Give the extent of all uninfected red blood cells.
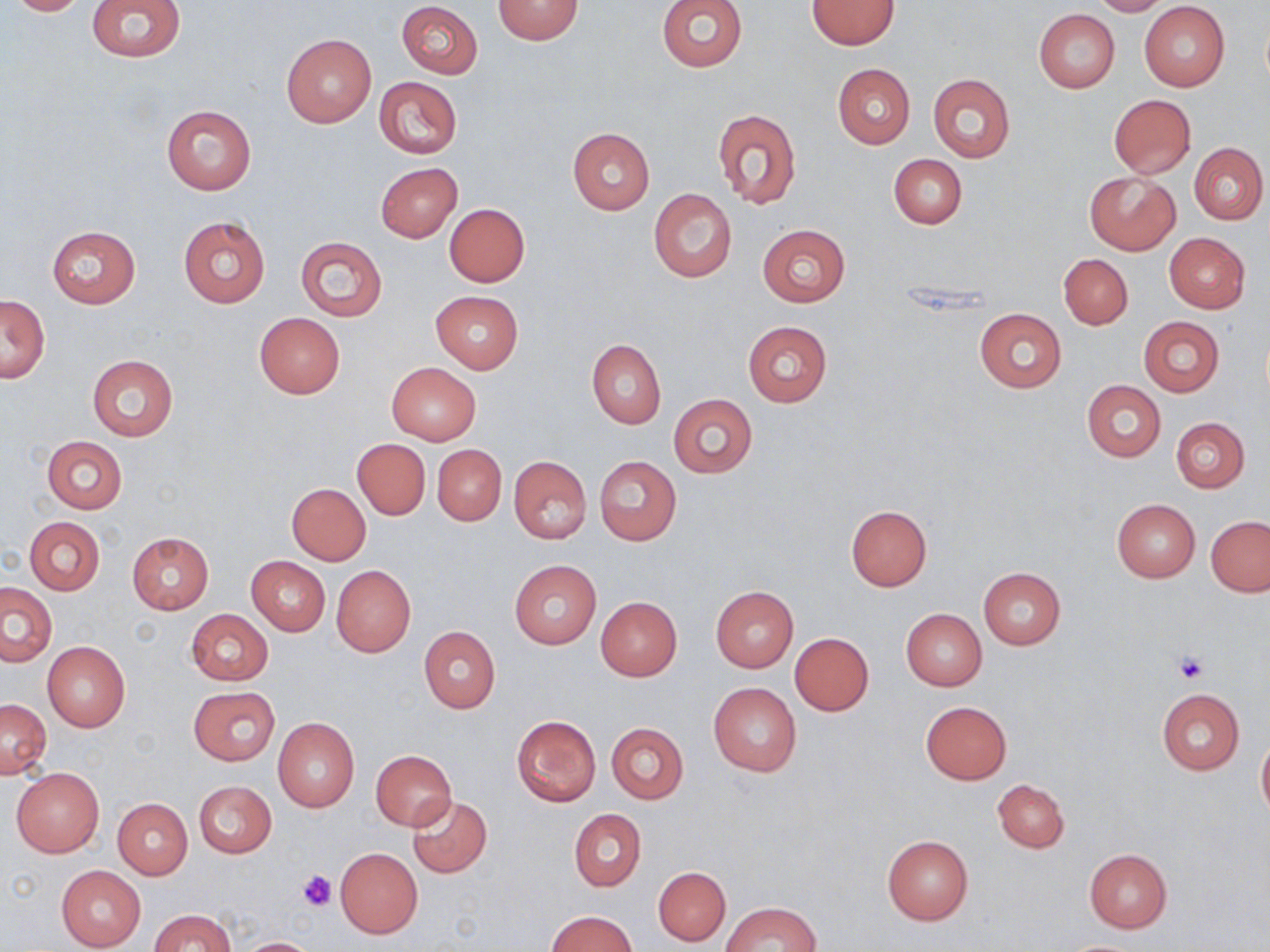

Approximate bounding boxes as [x1, y1, x2, y2] in pixels.
Uninfected red blood cells: [6, 0, 93, 16], [86, 0, 185, 61], [493, 0, 583, 43], [657, 0, 747, 72], [1090, 0, 1172, 16], [806, 1, 899, 50], [397, 2, 484, 78], [1139, 3, 1230, 92], [1034, 9, 1120, 93], [281, 34, 375, 128], [832, 63, 915, 149], [928, 74, 1015, 162], [372, 76, 461, 159], [1108, 94, 1196, 178], [161, 105, 256, 195], [712, 109, 802, 210], [568, 128, 655, 215], [1189, 142, 1268, 224], [888, 154, 966, 229], [375, 162, 462, 242], [1085, 172, 1180, 254], [649, 189, 737, 283], [444, 203, 530, 286], [177, 214, 271, 309], [758, 224, 851, 306], [47, 226, 139, 308], [1164, 233, 1250, 313], [294, 235, 389, 321], [1058, 253, 1133, 329], [431, 291, 523, 372], [1, 295, 50, 384], [973, 308, 1066, 394], [255, 312, 345, 399], [1138, 315, 1224, 397], [743, 321, 833, 407], [587, 340, 665, 428], [87, 354, 177, 441], [386, 362, 481, 444], [1081, 379, 1166, 462], [667, 394, 758, 479], [1171, 417, 1249, 492], [42, 435, 127, 513], [352, 439, 430, 519], [433, 444, 507, 526], [510, 455, 592, 543], [594, 455, 681, 546], [287, 483, 371, 565], [1111, 499, 1200, 581], [845, 505, 932, 592], [1206, 516, 1270, 596], [25, 517, 105, 595], [127, 532, 214, 613], [245, 556, 330, 636], [509, 560, 601, 648], [331, 565, 416, 657], [978, 567, 1065, 649], [1, 582, 56, 666], [710, 586, 799, 672], [595, 596, 681, 682], [186, 608, 273, 686], [900, 609, 987, 691], [418, 626, 501, 712], [790, 632, 874, 715], [41, 641, 130, 732], [709, 683, 802, 777], [186, 686, 279, 766], [1157, 688, 1245, 775], [1, 698, 51, 777], [921, 701, 1012, 784], [512, 716, 600, 805], [272, 717, 360, 812], [606, 723, 689, 803], [1256, 732, 1270, 823], [370, 750, 456, 831], [11, 768, 104, 857], [993, 779, 1070, 852], [194, 780, 276, 857], [407, 795, 491, 879], [114, 798, 192, 879], [569, 808, 646, 891], [882, 834, 973, 925], [335, 847, 422, 939], [1083, 848, 1172, 931], [55, 865, 145, 950], [654, 867, 730, 945], [722, 901, 820, 951], [151, 909, 233, 952], [546, 911, 638, 952], [238, 937, 323, 952].

Summary:
  - Platelet locations: [1173, 651, 1211, 684], [297, 869, 335, 910]
  - Slide-level diagnosis: no evidence of blood parasites
  - Stain: May-Grünwald-Giemsa
  - Modality: light microscopy
  - Preparation: thin blood film
  - Image size: 1270×952 pixels
  - Field of view: one of a larger specimen
  - Magnification: 1000x